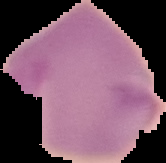

Image is 166×163 pixels. The area outside the segmented cell region is set to black. From a thin blood film. Result: negative for Plasmodium parasites.